Assess the morphology of the red blood cells.
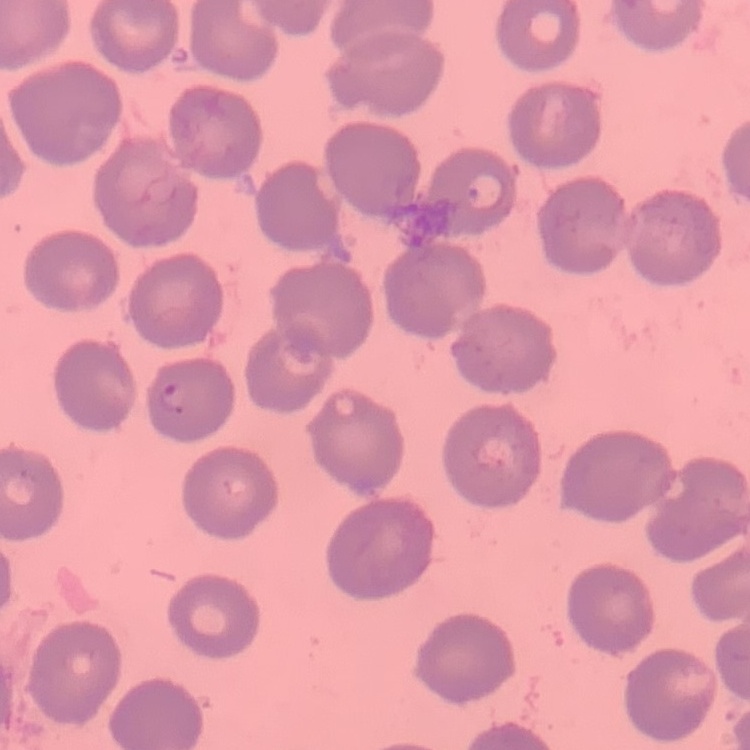

No rouleaux formation.

Summary:
  - Image type: one tile cut from a larger photomicrograph
  - Stain: Field's or Giemsa
  - Preparation: thin blood film